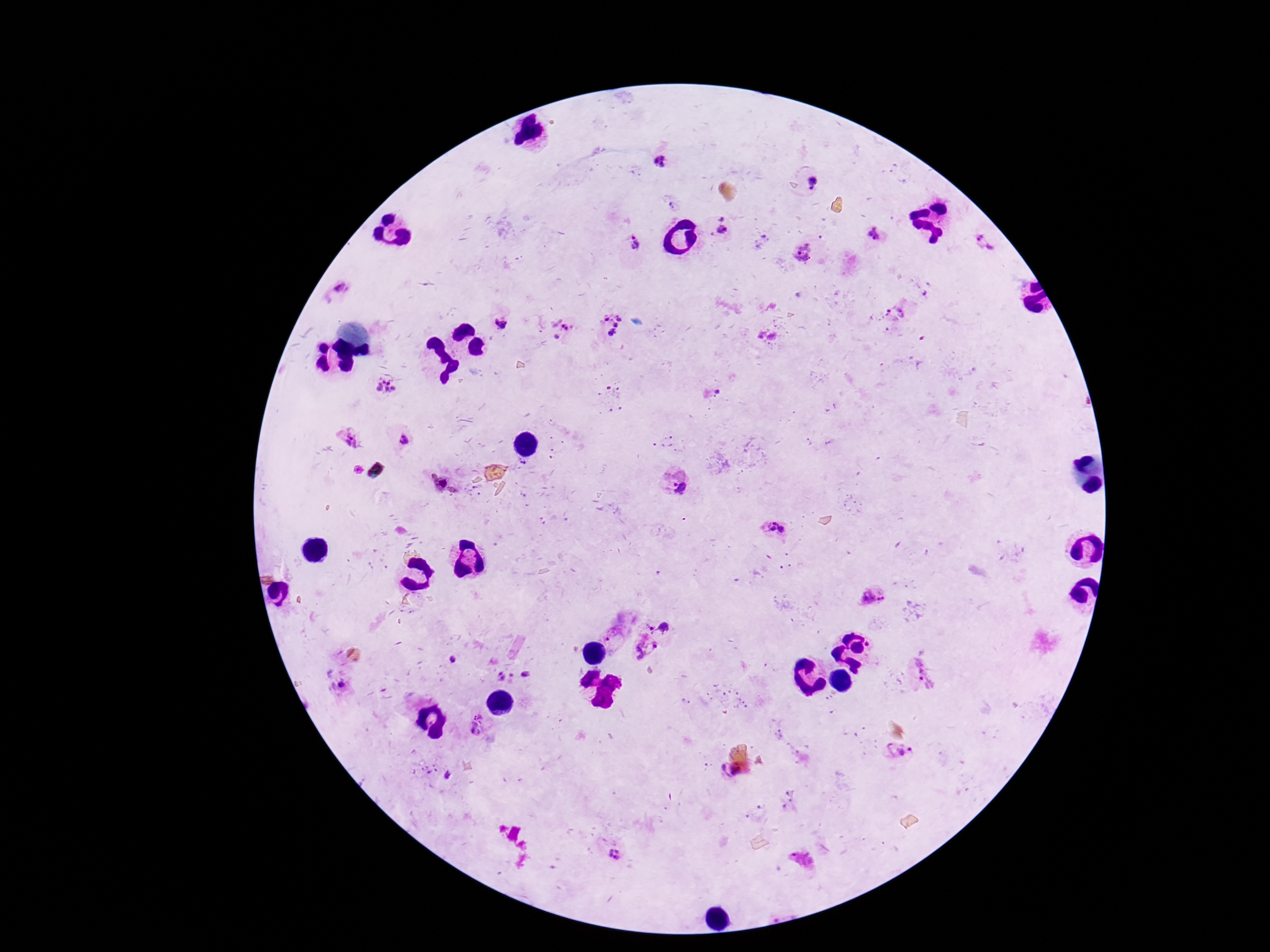 Approximate centers as [x, y] in pixels. Plasmodium parasite locations: [662, 162], [813, 183], [723, 227], [875, 233], [631, 240], [985, 244], [802, 252], [342, 290], [499, 323], [612, 325], [565, 331], [387, 386], [350, 438], [405, 440], [676, 483], [776, 530], [873, 595], [662, 627], [613, 640], [645, 649], [921, 672], [477, 726], [899, 753], [615, 855]. Giemsa-stained preparation. Image is 1270×952 pixels. Smartphone photograph taken through the microscope eyepiece. Patient malaria status: positive. Single field of view. Thick blood smear. 100x magnification.